Report the malaria status of this cell.
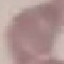
It is uninfected.

Summary:
  - Stain: Giemsa
  - Capture: smartphone camera at the microscope eyepiece
  - Image type: cell patch, automatically extracted from a larger field of view and resized to 64 × 64 pixels
  - Preparation: thin blood film